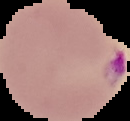 From a thin blood film. Image is 130×121 pixels. Malaria status: parasitized. Segmented cell region on a black background.